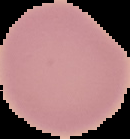
Segmented cell region on a black background. Image is 130×139 pixels. Malaria status: uninfected. From a thin blood smear.